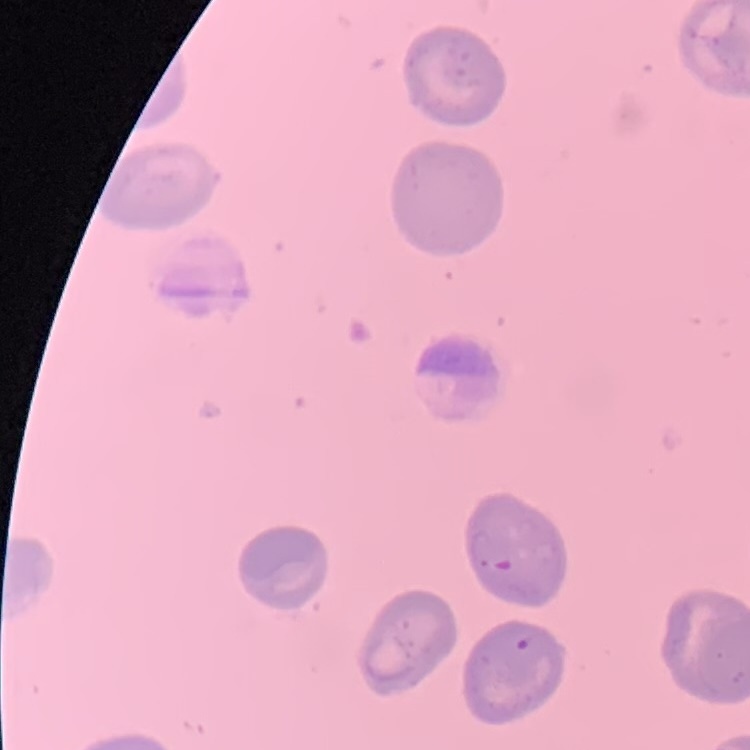
The red blood cells exhibit no rouleaux formation. Field's or Giemsa stain. Thin blood smear. One tile cut from a larger photomicrograph.